Locate every leukocyte (white blood cell).
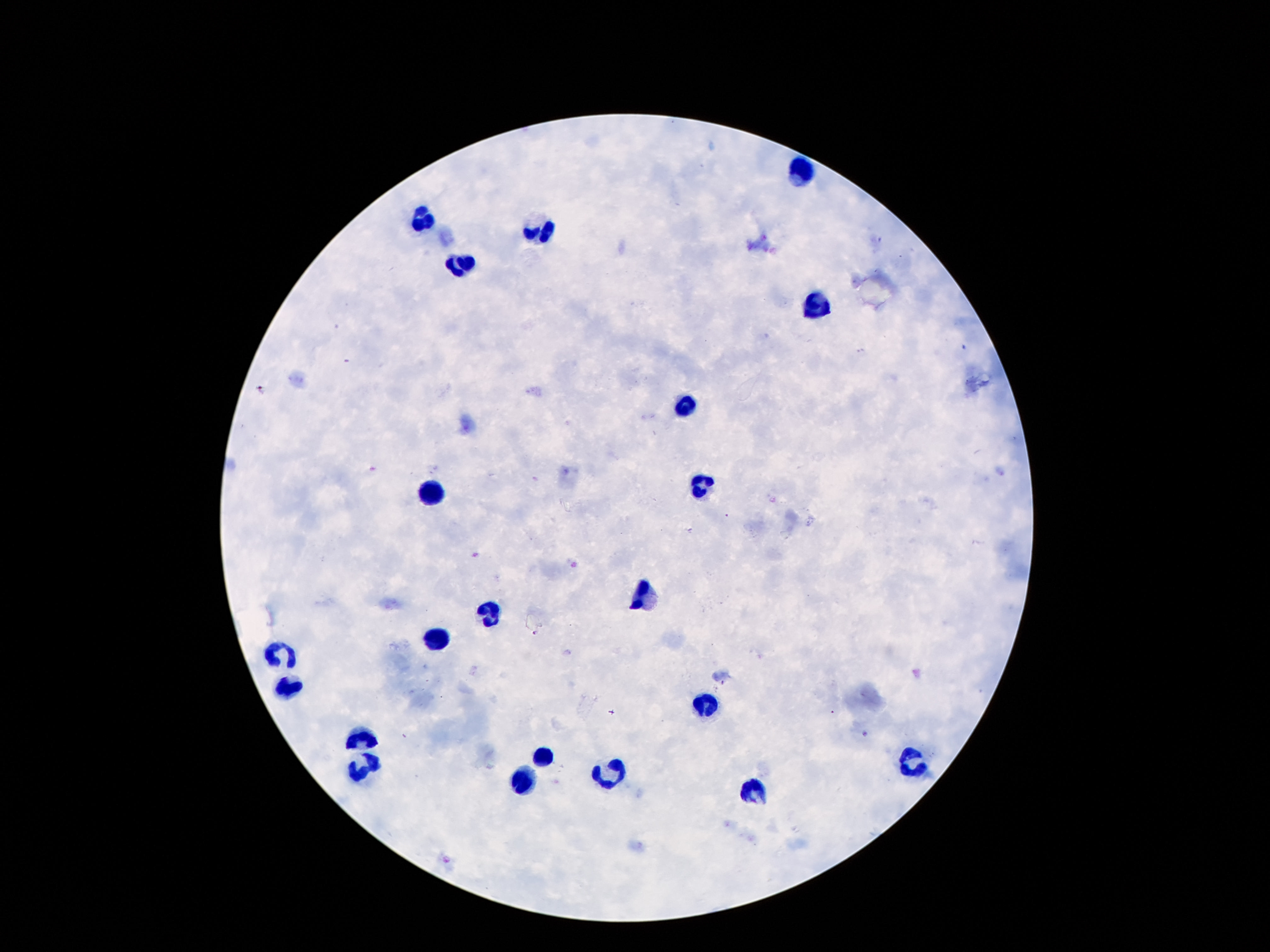
Approximate centers as {x, y} in pixels.
Leukocytes: {802, 169}, {418, 219}, {541, 229}, {457, 264}, {814, 305}, {685, 406}, {432, 485}, {700, 485}, {643, 597}, {494, 613}, {436, 640}, {282, 658}, {291, 690}, {702, 703}, {362, 734}, {543, 758}, {916, 762}, {362, 769}, {609, 773}, {524, 779}, {751, 788}.

Summary:
  - Image size: 1270×952 pixels
  - Magnification: 100x
  - Capture: smartphone camera through the microscope eyepiece
  - Preparation: thick blood smear
  - Field of view: one from this slide
  - Stain: Giemsa
  - Patient malaria status: not infected